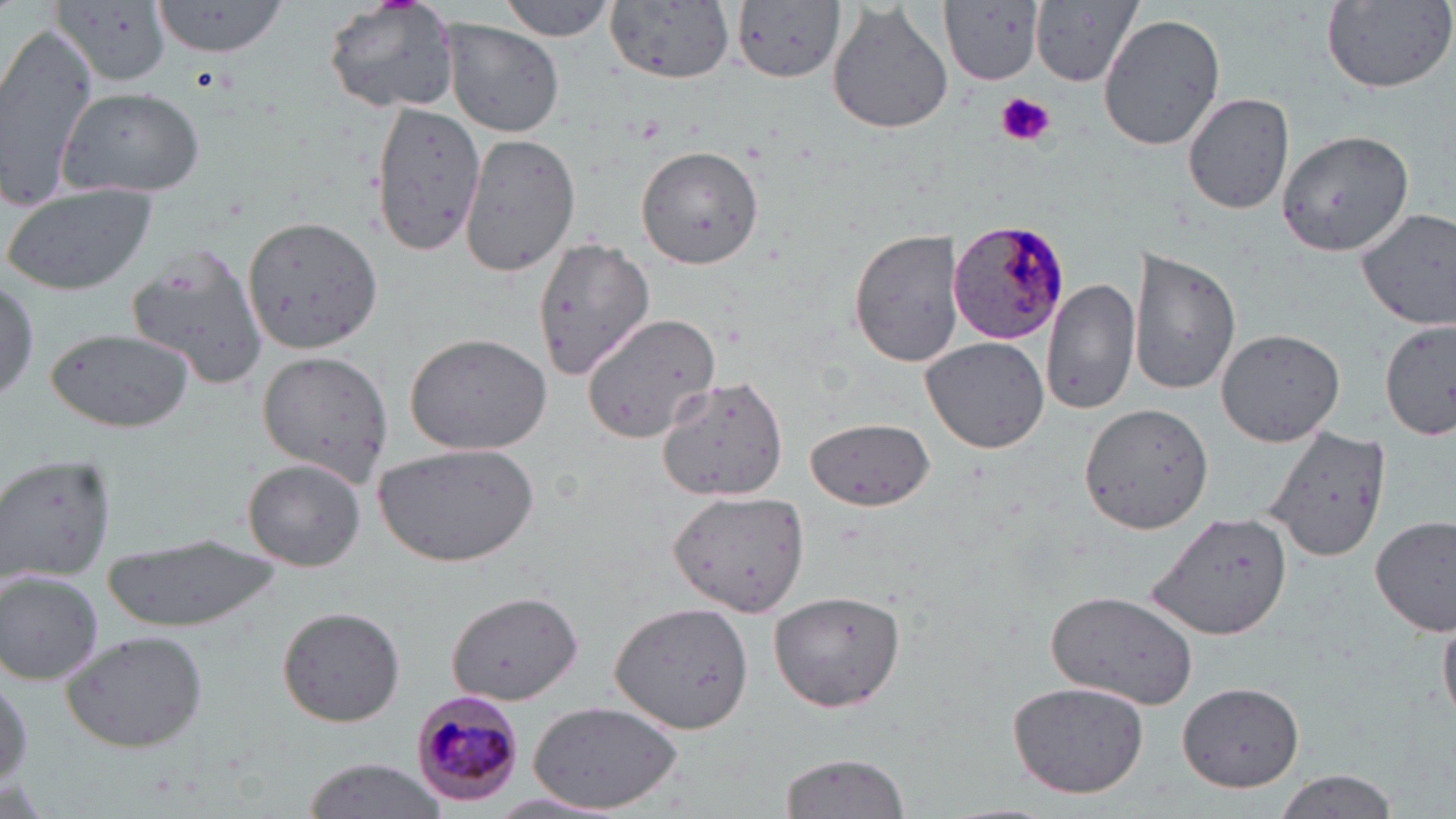

Summary:
  - Coordinate format: approximate bounding boxes as (x1, y1, x2, y2) in pixels
  - Uninfected red blood cell locations: (150, 0, 289, 57), (323, 0, 461, 114), (497, 0, 619, 41), (606, 0, 733, 84), (942, 0, 1045, 85), (1319, 0, 1454, 93), (54, 1, 170, 86), (730, 1, 850, 83), (827, 1, 954, 136), (1031, 1, 1143, 86), (1097, 13, 1225, 153), (442, 18, 564, 136), (0, 22, 98, 209), (59, 87, 206, 198), (1182, 92, 1295, 215), (370, 103, 483, 257), (1279, 129, 1415, 259), (461, 132, 583, 276), (637, 144, 763, 267), (1, 184, 156, 295), (1355, 207, 1456, 332), (244, 215, 381, 353), (849, 229, 965, 366), (532, 235, 657, 377), (125, 245, 269, 389), (1131, 247, 1242, 397), (0, 275, 40, 405), (1040, 276, 1138, 416), (580, 311, 722, 445), (1379, 320, 1455, 442), (1215, 327, 1346, 446), (44, 328, 194, 434), (403, 331, 553, 456), (920, 337, 1050, 454), (255, 351, 394, 487), (652, 374, 792, 503), (1080, 402, 1213, 535), (804, 416, 935, 510), (1263, 424, 1392, 564), (376, 443, 539, 567), (1, 452, 117, 581), (241, 459, 366, 570), (668, 488, 814, 618), (1148, 512, 1295, 641), (1372, 515, 1455, 637), (99, 533, 283, 631), (2, 573, 103, 684), (768, 588, 908, 714), (444, 589, 586, 704), (1045, 589, 1201, 710), (612, 601, 753, 735), (275, 604, 406, 726), (1439, 612, 1455, 729), (61, 630, 211, 753), (0, 669, 32, 796), (1007, 679, 1150, 798), (1176, 682, 1309, 791), (527, 701, 687, 814), (777, 751, 913, 819), (300, 760, 451, 816), (1269, 769, 1399, 819)
  - Plasmodium malariae-infected red blood cell locations: (945, 214, 1071, 346), (409, 684, 526, 807)
  - Platelet locations: (995, 92, 1055, 147)
  - Slide-level diagnosis: Plasmodium malariae
  - Modality: optical microscopy
  - Field of view: single
  - Preparation: thin blood film
  - Stain: May-Grünwald-Giemsa
  - Image size: 1456×819 pixels
  - Magnification: 1000x